Report the malaria status of this cell.
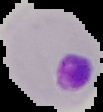
Parasitized.

image size = 103×112 pixels
preparation = thin blood film
image type = segmented cell region on a black background